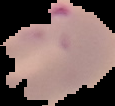

The area outside the segmented cell region is set to black. From a thin blood film. Malaria status: parasitized. Image is 115×106 pixels.